State which parasite is depicted.
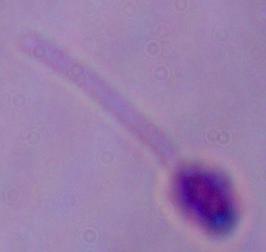
This is Leishmania.

magnification: 1000x
modality: photomicrograph